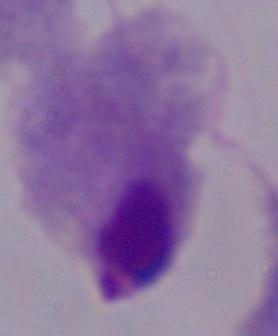
modality = micrograph
identification = trichomonad
magnification = 1000x